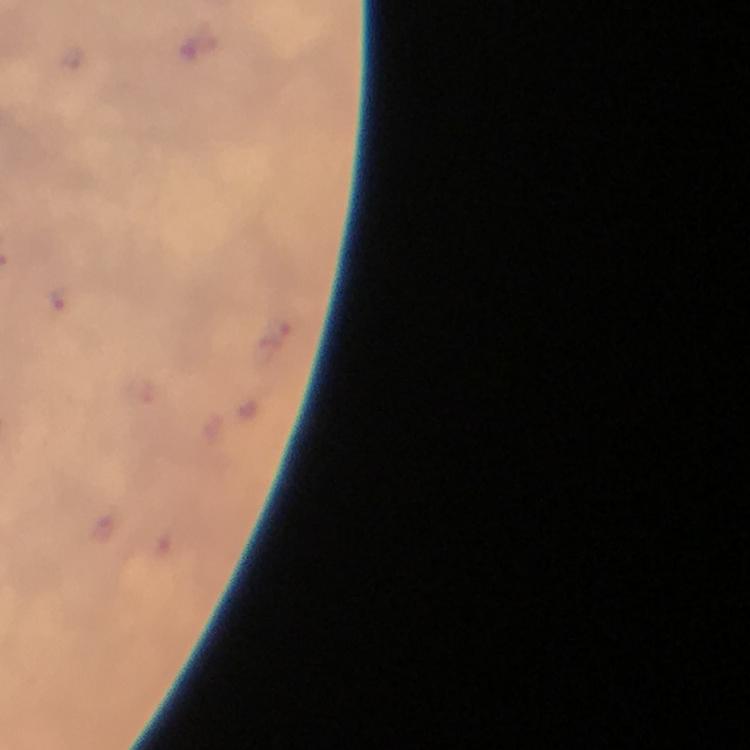
Approximate centers as [x, y] in pixels.
Summary:
  - Plasmodium parasite locations: [61, 298]
  - Preparation: thick smear
  - Cropped from: a single field of view
  - Immersion oil: used
  - Magnification: 100x
  - Capture: smartphone camera through the microscope
  - Stain: Giemsa
  - Context: from a malaria diagnostic workup
  - Image size: 750×750 pixels